Name the parasite shown.
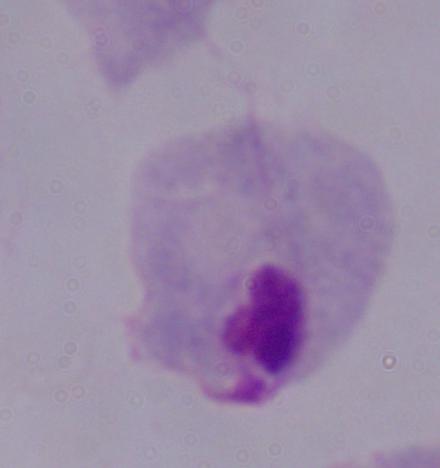
This is a trichomonad.

Photomicrograph. Captured at 1000x magnification.